Describe the morphology of the erythrocytes.
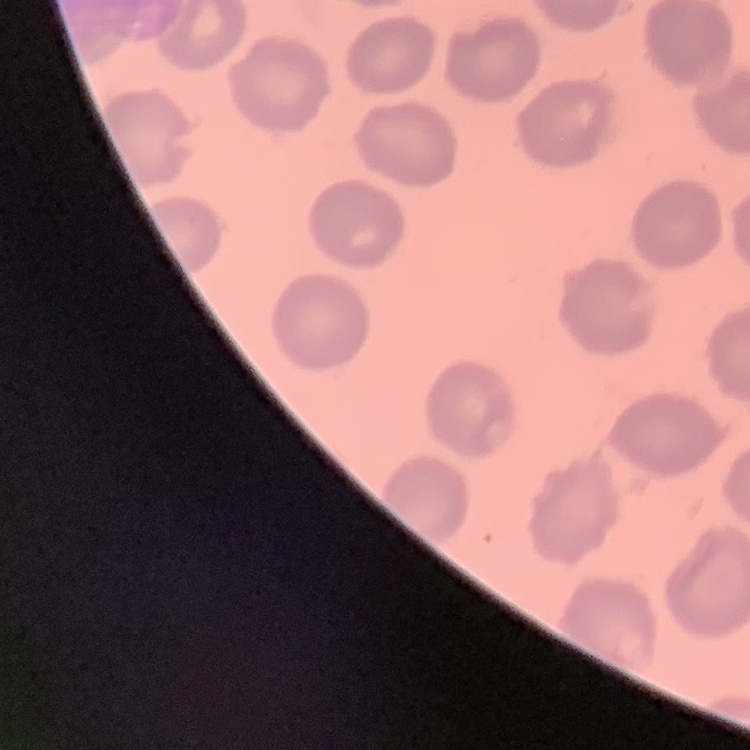
No rouleaux formation.

image_type: one tile cut from a larger photomicrograph
preparation: thin blood smear
stain: Field's or Giemsa